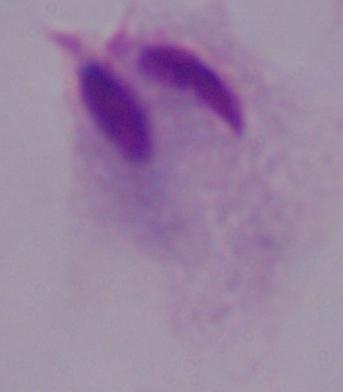

Summary:
  - Magnification: 1000x
  - Modality: micrograph
  - Identification: trichomonad